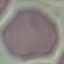

{
  "malaria_status": "uninfected",
  "stain": "Giemsa",
  "preparation": "thin blood film",
  "capture": "smartphone through the microscope eyepiece",
  "image_type": "automatically extracted cell patch, resized to 64 × 64 pixels"
}